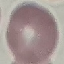
Summary:
  - Result: no malaria parasites seen
  - Preparation: thin blood smear
  - Capture: smartphone camera at the microscope eyepiece
  - Image type: automatically extracted cell patch, resized to 64 × 64 pixels
  - Stain: Giemsa